Identify the parasite.
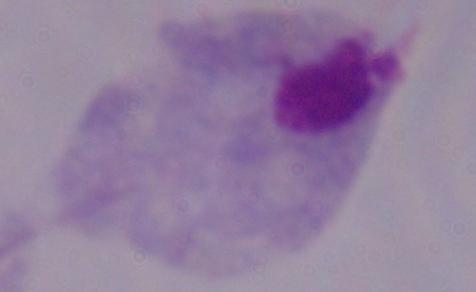

This is a trichomonad.

1000x magnification. Photomicrograph.